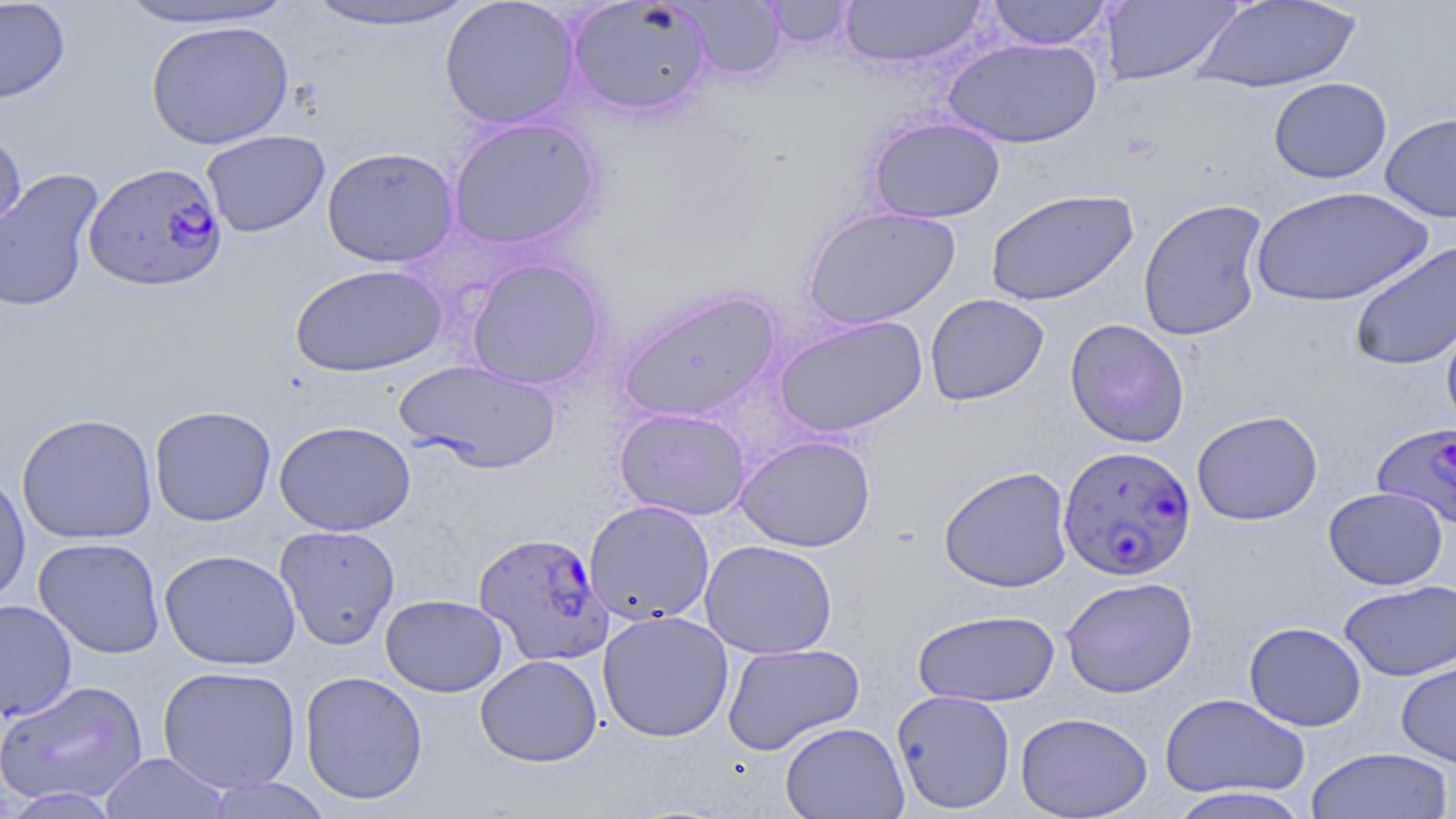

Summary:
  - Coordinate format: approximate bounding boxes as (x1, y1, x2, y2) in pixels
  - Uninfected red blood cell locations: (0, 0, 71, 105), (111, 0, 301, 31), (439, 0, 582, 131), (566, 0, 712, 118), (678, 0, 785, 81), (838, 0, 987, 69), (985, 0, 1113, 50), (1193, 0, 1362, 92), (297, 1, 485, 32), (762, 1, 856, 49), (1099, 1, 1243, 85), (145, 20, 295, 149), (943, 37, 1103, 149), (1268, 77, 1392, 184), (1380, 111, 1456, 223), (868, 115, 1005, 223), (447, 117, 601, 250), (0, 125, 27, 245), (201, 130, 330, 237), (321, 147, 459, 268), (0, 168, 105, 312), (1251, 186, 1432, 308), (985, 189, 1138, 307), (1137, 198, 1270, 341), (801, 205, 960, 330), (1348, 241, 1456, 372), (466, 257, 606, 390), (289, 263, 447, 378), (617, 288, 781, 423), (924, 293, 1049, 406), (1441, 310, 1456, 439), (774, 315, 927, 437), (1065, 318, 1190, 448), (396, 359, 561, 473), (149, 405, 277, 526), (614, 407, 751, 520), (1191, 410, 1323, 525), (16, 412, 158, 544), (274, 420, 416, 536), (735, 434, 875, 552), (938, 465, 1074, 593), (0, 470, 31, 608), (1323, 486, 1448, 590), (584, 500, 715, 626), (275, 525, 401, 650), (33, 537, 166, 659), (699, 539, 837, 659), (159, 548, 301, 670), (1060, 576, 1198, 699), (1338, 579, 1456, 682), (380, 593, 507, 697), (0, 598, 77, 721), (912, 609, 1060, 707), (597, 610, 734, 742), (1243, 621, 1367, 731), (722, 643, 865, 755), (475, 654, 603, 767), (1396, 661, 1456, 768), (157, 665, 302, 792), (299, 670, 429, 806), (1, 679, 148, 808), (891, 689, 1016, 813), (1159, 692, 1310, 798), (1015, 711, 1153, 818), (779, 721, 909, 819), (1305, 746, 1453, 819), (99, 752, 230, 818), (205, 776, 333, 818), (1164, 786, 1314, 819)
  - Plasmodium falciparum-infected red blood cell locations: (83, 161, 228, 291), (1372, 422, 1456, 531), (1057, 448, 1197, 586), (474, 531, 612, 666)
  - Slide-level diagnosis: Plasmodium falciparum
  - Image size: 1456×819 pixels
  - Preparation: thin blood film
  - Magnification: 1000x
  - Stain: May-Grünwald-Giemsa
  - Field of view: one of a larger specimen
  - Modality: optical microscopy